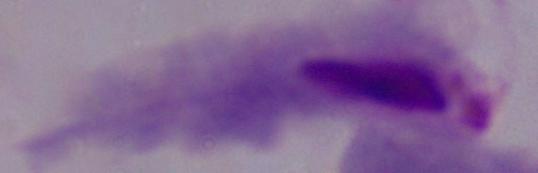
Summary:
  - Magnification: 1000x
  - Identification: trichomonad
  - Modality: micrograph